Locate every Plasmodium parasite.
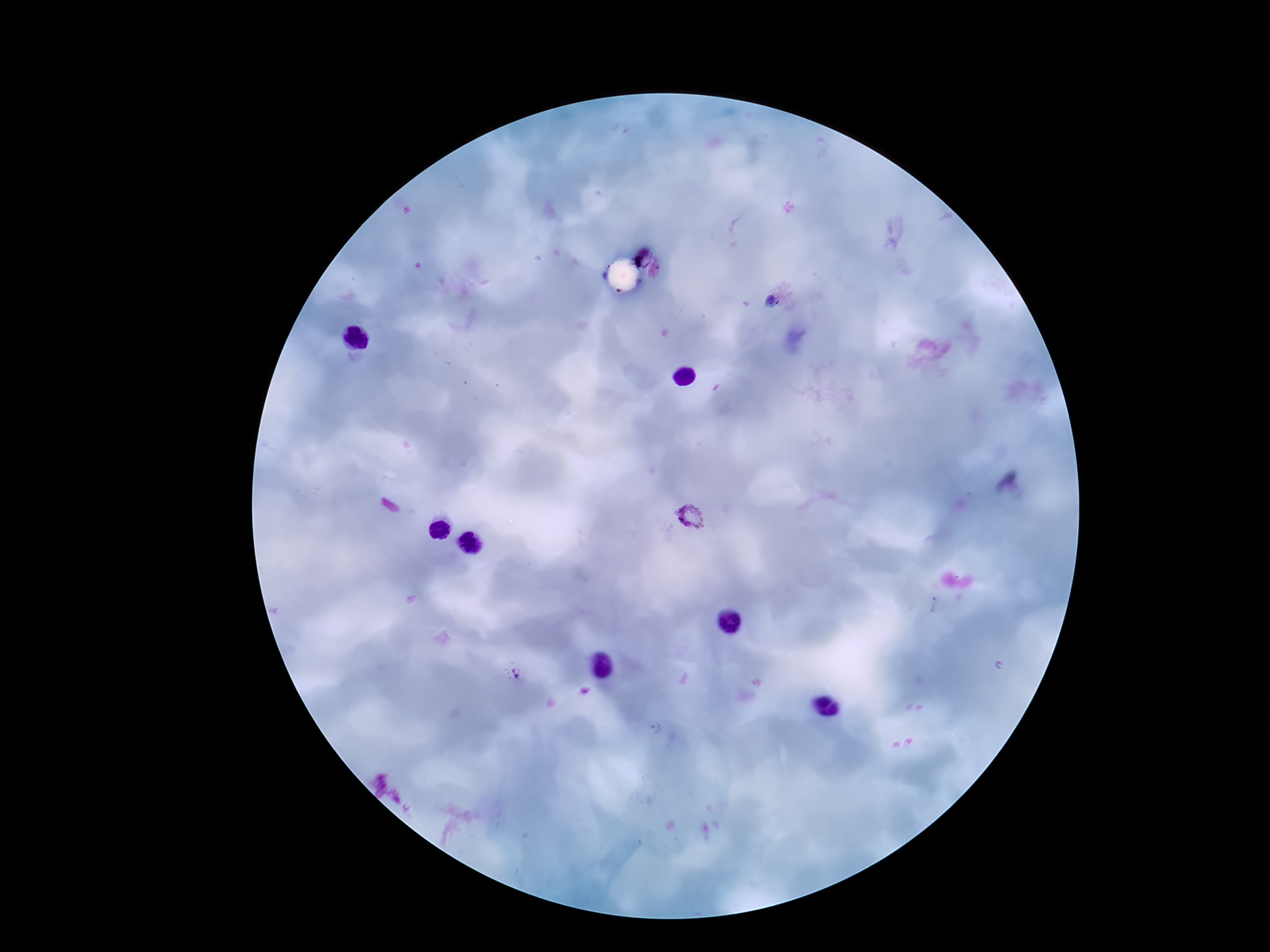

Approximate object centers, in pixels from the top-left corner.
Plasmodium parasites: (x=690, y=518), (x=933, y=606), (x=518, y=675), (x=655, y=730).

Smartphone photograph taken through the microscope eyepiece. Giemsa stain. One field from this slide. 100x magnification. Image is 1270×952 pixels. Patient malaria status: infected. Thick blood film.